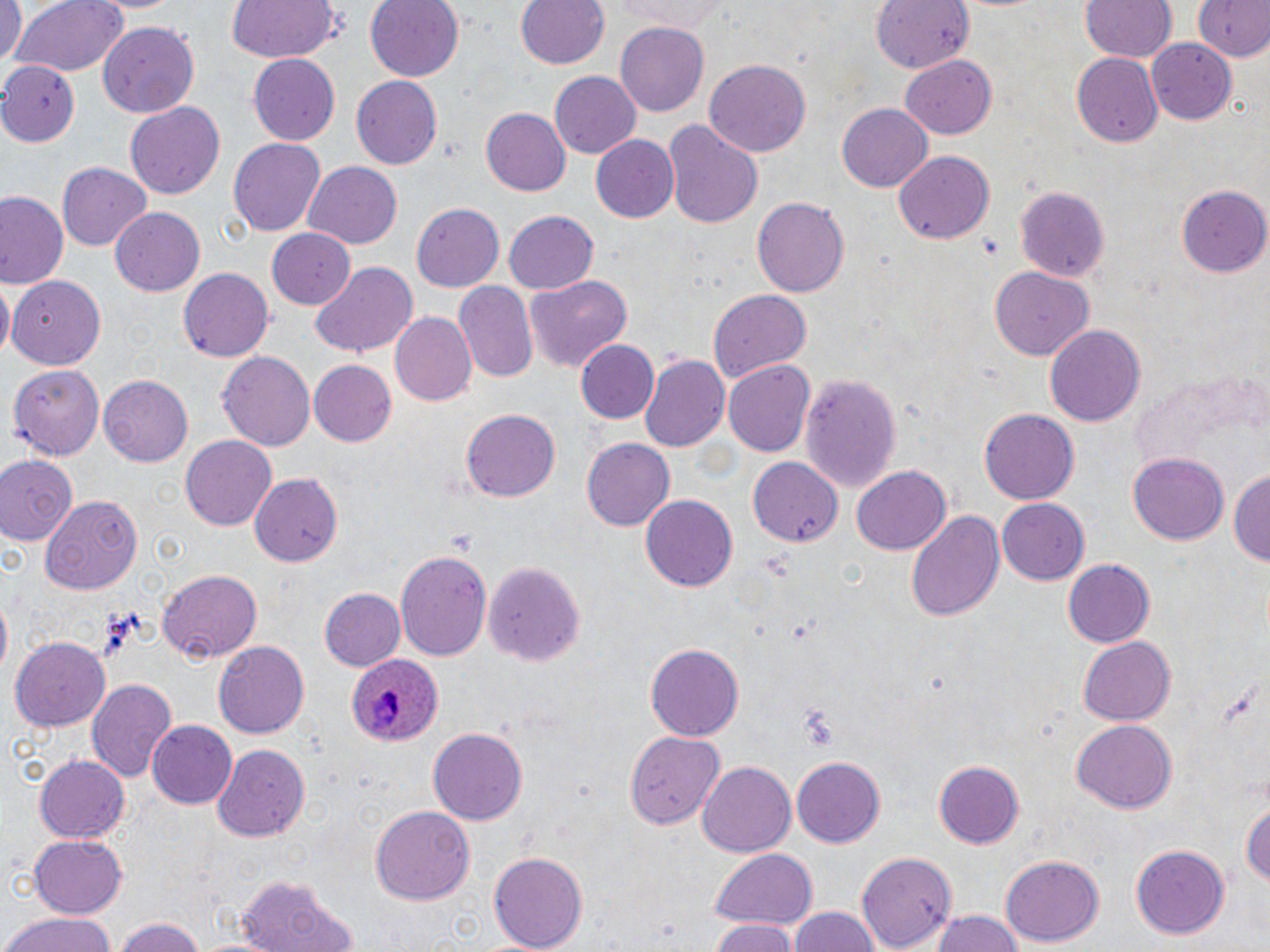 Approximate bounding boxes as named x1/y1/x2/y2 corners in pixels. Plasmodium ovale-infected red blood cell locations: (x1=347, y1=652, x2=443, y2=746). Uninfected red blood cell locations: (x1=0, y1=0, x2=26, y2=72), (x1=10, y1=0, x2=129, y2=79), (x1=222, y1=0, x2=339, y2=64), (x1=364, y1=0, x2=465, y2=84), (x1=516, y1=0, x2=609, y2=71), (x1=609, y1=0, x2=730, y2=32), (x1=869, y1=0, x2=974, y2=75), (x1=1081, y1=0, x2=1176, y2=63), (x1=1194, y1=0, x2=1269, y2=62), (x1=614, y1=21, x2=709, y2=117), (x1=100, y1=22, x2=200, y2=118), (x1=1147, y1=41, x2=1236, y2=123), (x1=248, y1=53, x2=340, y2=144), (x1=1073, y1=55, x2=1163, y2=147), (x1=902, y1=56, x2=997, y2=138), (x1=241, y1=60, x2=425, y2=151), (x1=704, y1=61, x2=812, y2=159), (x1=0, y1=63, x2=81, y2=144), (x1=550, y1=71, x2=640, y2=158), (x1=352, y1=76, x2=443, y2=167), (x1=125, y1=101, x2=228, y2=199), (x1=837, y1=102, x2=933, y2=193), (x1=482, y1=106, x2=571, y2=198), (x1=663, y1=118, x2=763, y2=228), (x1=591, y1=135, x2=679, y2=223), (x1=227, y1=138, x2=325, y2=236), (x1=895, y1=152, x2=994, y2=244), (x1=57, y1=162, x2=151, y2=249), (x1=301, y1=162, x2=403, y2=248), (x1=1180, y1=185, x2=1270, y2=277), (x1=2, y1=186, x2=77, y2=369), (x1=1015, y1=186, x2=1108, y2=283), (x1=0, y1=191, x2=66, y2=288), (x1=752, y1=198, x2=848, y2=299), (x1=412, y1=202, x2=504, y2=290), (x1=110, y1=206, x2=204, y2=295), (x1=505, y1=210, x2=598, y2=293), (x1=265, y1=227, x2=355, y2=308), (x1=310, y1=262, x2=419, y2=358), (x1=178, y1=267, x2=275, y2=363), (x1=991, y1=267, x2=1094, y2=360), (x1=523, y1=274, x2=633, y2=370), (x1=8, y1=276, x2=108, y2=370), (x1=1, y1=281, x2=14, y2=357), (x1=455, y1=281, x2=540, y2=383), (x1=707, y1=288, x2=812, y2=383), (x1=390, y1=312, x2=477, y2=408), (x1=1044, y1=323, x2=1146, y2=429), (x1=575, y1=339, x2=658, y2=423), (x1=218, y1=350, x2=315, y2=449), (x1=641, y1=353, x2=733, y2=454), (x1=309, y1=360, x2=396, y2=446), (x1=9, y1=361, x2=103, y2=455), (x1=723, y1=361, x2=814, y2=458), (x1=800, y1=374, x2=901, y2=495), (x1=100, y1=375, x2=196, y2=465), (x1=461, y1=408, x2=561, y2=503), (x1=979, y1=409, x2=1077, y2=506), (x1=181, y1=435, x2=277, y2=532), (x1=581, y1=438, x2=675, y2=532), (x1=1127, y1=452, x2=1228, y2=546), (x1=0, y1=453, x2=79, y2=548), (x1=748, y1=457, x2=846, y2=546), (x1=852, y1=466, x2=951, y2=554), (x1=1230, y1=468, x2=1269, y2=572), (x1=249, y1=472, x2=342, y2=565), (x1=41, y1=496, x2=143, y2=593), (x1=640, y1=496, x2=737, y2=592), (x1=996, y1=497, x2=1088, y2=585), (x1=904, y1=509, x2=1004, y2=623), (x1=394, y1=549, x2=493, y2=662), (x1=1059, y1=556, x2=1155, y2=650), (x1=486, y1=559, x2=587, y2=666), (x1=158, y1=571, x2=262, y2=662), (x1=321, y1=587, x2=404, y2=669), (x1=11, y1=638, x2=110, y2=730), (x1=1078, y1=638, x2=1175, y2=723), (x1=213, y1=639, x2=309, y2=738), (x1=642, y1=642, x2=743, y2=741), (x1=85, y1=677, x2=177, y2=781), (x1=1072, y1=718, x2=1177, y2=812), (x1=148, y1=721, x2=239, y2=809), (x1=427, y1=726, x2=528, y2=825), (x1=626, y1=731, x2=731, y2=834), (x1=211, y1=742, x2=310, y2=841), (x1=35, y1=752, x2=131, y2=842), (x1=790, y1=756, x2=886, y2=847), (x1=932, y1=759, x2=1024, y2=849), (x1=697, y1=763, x2=795, y2=856), (x1=1240, y1=795, x2=1269, y2=896), (x1=370, y1=805, x2=475, y2=905), (x1=28, y1=837, x2=128, y2=917), (x1=1128, y1=844, x2=1231, y2=941), (x1=709, y1=847, x2=818, y2=931), (x1=487, y1=850, x2=589, y2=952), (x1=858, y1=851, x2=954, y2=952), (x1=1001, y1=855, x2=1104, y2=947), (x1=234, y1=873, x2=352, y2=952), (x1=786, y1=907, x2=883, y2=952), (x1=929, y1=910, x2=1026, y2=952), (x1=1, y1=913, x2=121, y2=952), (x1=111, y1=916, x2=212, y2=952), (x1=709, y1=922, x2=802, y2=952). Slide-level diagnosis: Plasmodium ovale. Image is 1270×952 pixels. Single field of view. Captured at 1000x magnification. Optical microscopy. Thin blood smear. May-Grünwald-Giemsa stain.